Report the malaria status.
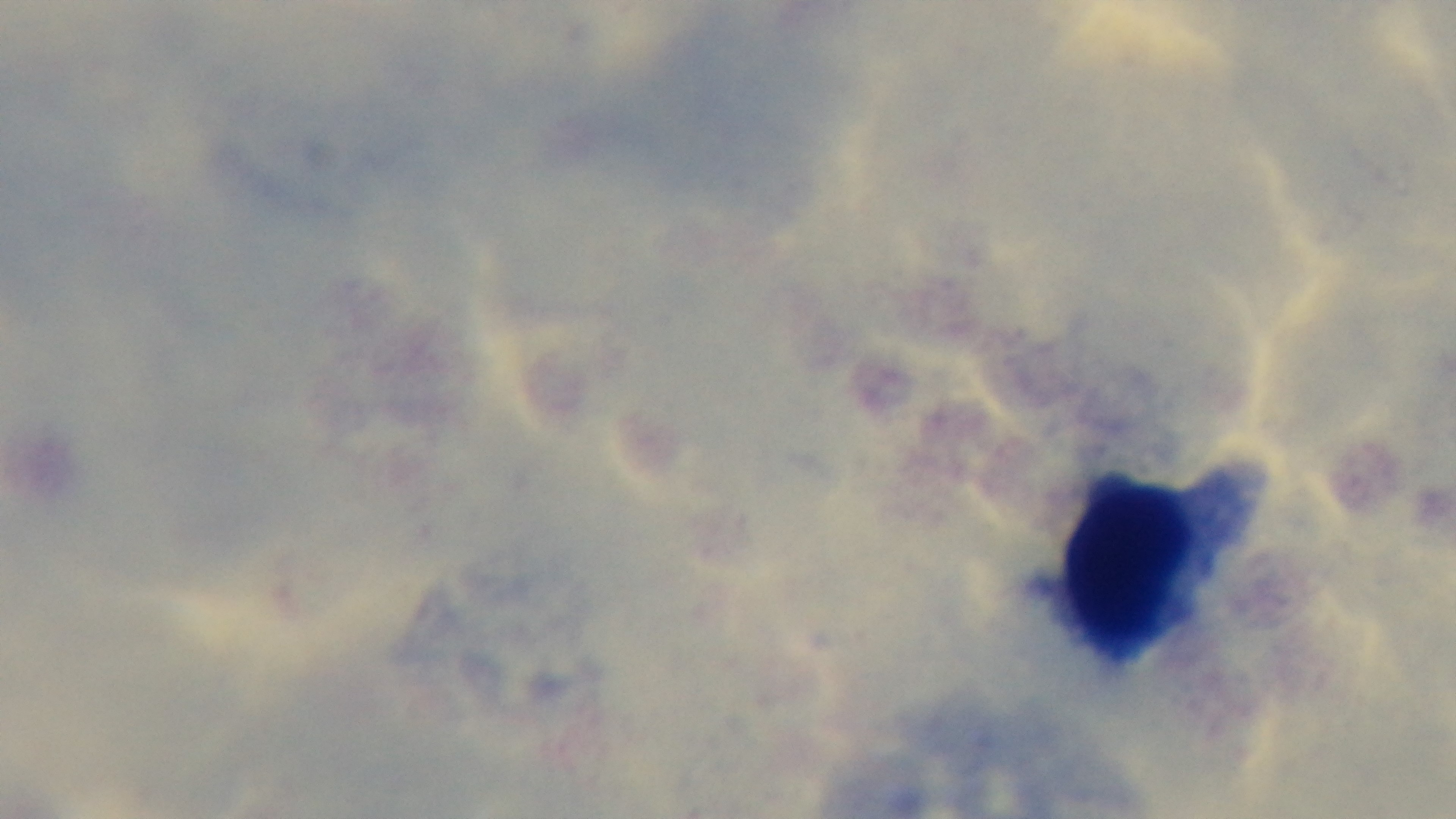
It is uninfected.

stain = Giemsa
field of view = single
modality = light microscopy
preparation = thick smear
objective = 100x oil immersion
capture = mounted 4K digital camera